Classify this cell by malaria status.
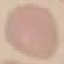
Uninfected.

image type = cell patch, automatically extracted from a larger field of view and resized to 64 × 64 pixels
capture = smartphone camera at the microscope eyepiece
stain = Giemsa
preparation = thin smear